Point out each leukocyte.
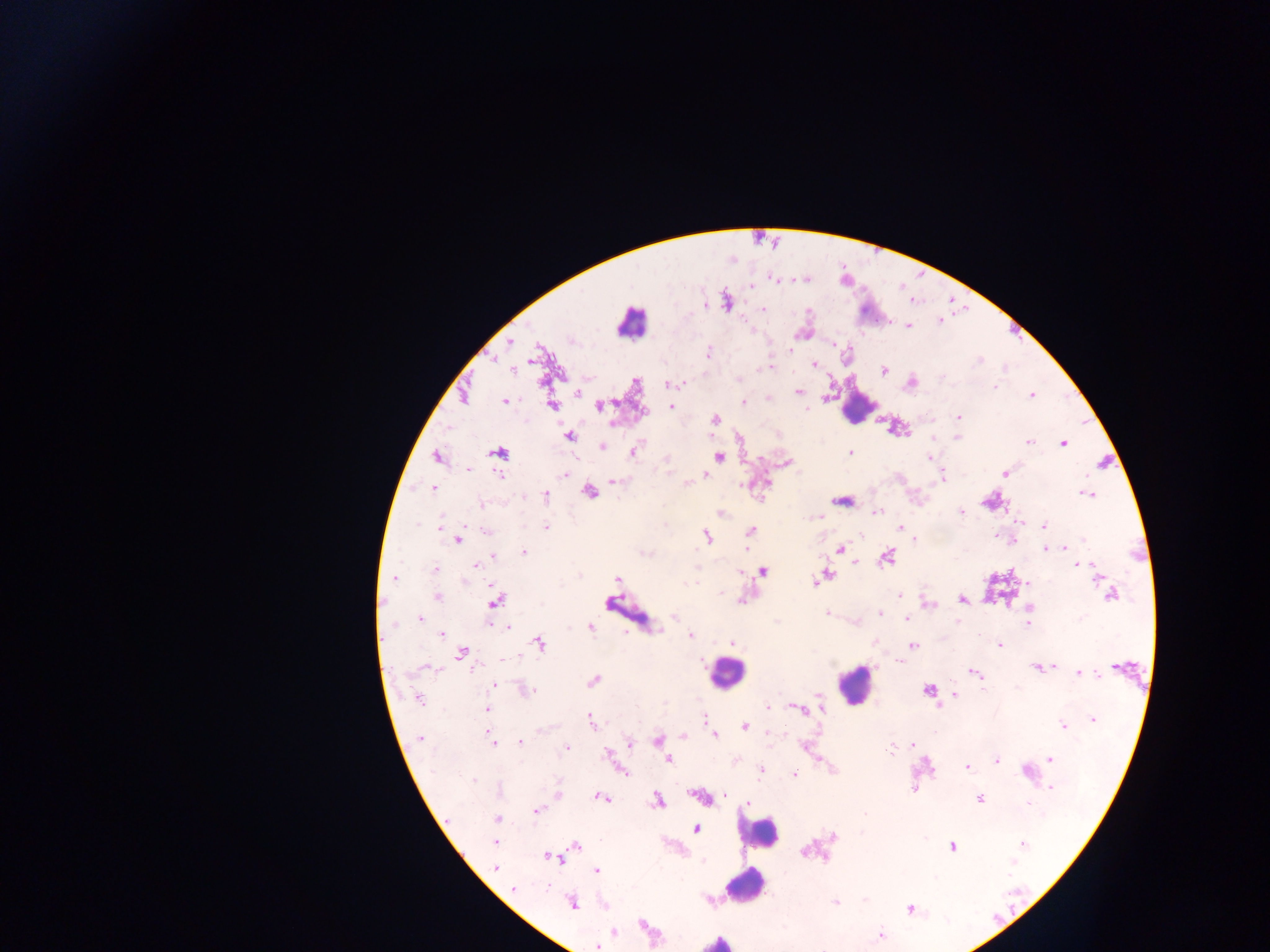

Approximate centers as (x, y) in pixels.
Leukocytes: (631, 322), (856, 410), (726, 673), (855, 684), (760, 833), (745, 885), (717, 941).

Summary:
  - Plasmodium parasite locations: (775, 279), (751, 286), (727, 304), (704, 305), (763, 309), (940, 320), (908, 326), (510, 342), (791, 349), (709, 352), (532, 358), (979, 360), (814, 364), (769, 367), (764, 368), (511, 369), (884, 371), (911, 383), (669, 384), (995, 387), (798, 391), (578, 392), (1032, 395), (768, 399), (505, 401), (743, 403), (551, 405), (600, 405), (671, 406), (959, 417), (714, 420), (570, 436), (957, 438), (1029, 442), (1063, 443), (602, 446), (635, 451), (499, 452), (850, 452), (930, 456), (719, 457), (437, 458), (787, 463), (468, 469), (1005, 473), (565, 474), (500, 475), (706, 476), (942, 476), (614, 482), (687, 484), (433, 488), (589, 492), (1087, 494), (545, 495), (841, 500), (482, 505), (721, 512), (876, 512), (962, 512), (820, 516), (1019, 521), (417, 524), (1044, 525), (441, 526), (547, 527), (901, 528), (486, 530), (750, 531), (707, 536), (996, 536), (458, 540), (1083, 540), (1065, 548), (747, 549), (841, 550), (1045, 550), (524, 552), (643, 553), (494, 557), (887, 558), (854, 563), (477, 565), (1083, 565), (1092, 566), (434, 570), (763, 572), (825, 576), (395, 578), (617, 579), (814, 582), (692, 584), (1104, 589), (721, 593), (1111, 595), (899, 596), (437, 597), (496, 600), (741, 600), (962, 600), (929, 604), (1029, 608), (826, 613), (880, 613), (674, 617), (420, 618), (907, 618), (957, 621), (1028, 623), (507, 626), (590, 628), (441, 634), (690, 635), (540, 643), (733, 643), (913, 645), (999, 645), (461, 653), (504, 658), (900, 661), (1053, 666), (473, 667), (424, 668), (1036, 668), (974, 672), (1080, 673), (593, 681), (495, 686), (526, 690), (928, 690), (955, 695), (419, 699), (820, 699), (768, 707), (796, 708), (486, 709), (704, 718), (1093, 719), (590, 721), (1063, 726), (744, 727), (770, 732), (715, 735), (683, 736), (420, 739), (492, 740), (658, 741), (521, 742), (630, 743), (913, 744), (805, 746), (566, 749), (891, 749), (663, 751), (606, 755), (1050, 759), (669, 761), (996, 761), (967, 767), (761, 770), (623, 772), (1026, 772), (794, 775), (473, 780), (1051, 788), (914, 789), (558, 794), (726, 796), (698, 797), (603, 798), (980, 799), (657, 801), (749, 803), (1029, 803), (537, 810), (864, 814), (497, 818), (695, 829), (833, 836), (495, 843), (1023, 843), (575, 846), (952, 847), (805, 851), (550, 858), (1011, 863), (496, 867), (597, 871), (548, 887), (513, 888), (572, 903), (836, 903), (910, 909), (642, 925), (614, 932), (880, 935), (597, 946)
  - Country: Ghana
  - Preparation: thick blood smear
  - Capture: mobile-phone photograph through a microscope
  - Image size: 1270×952 pixels
  - Field of view: single